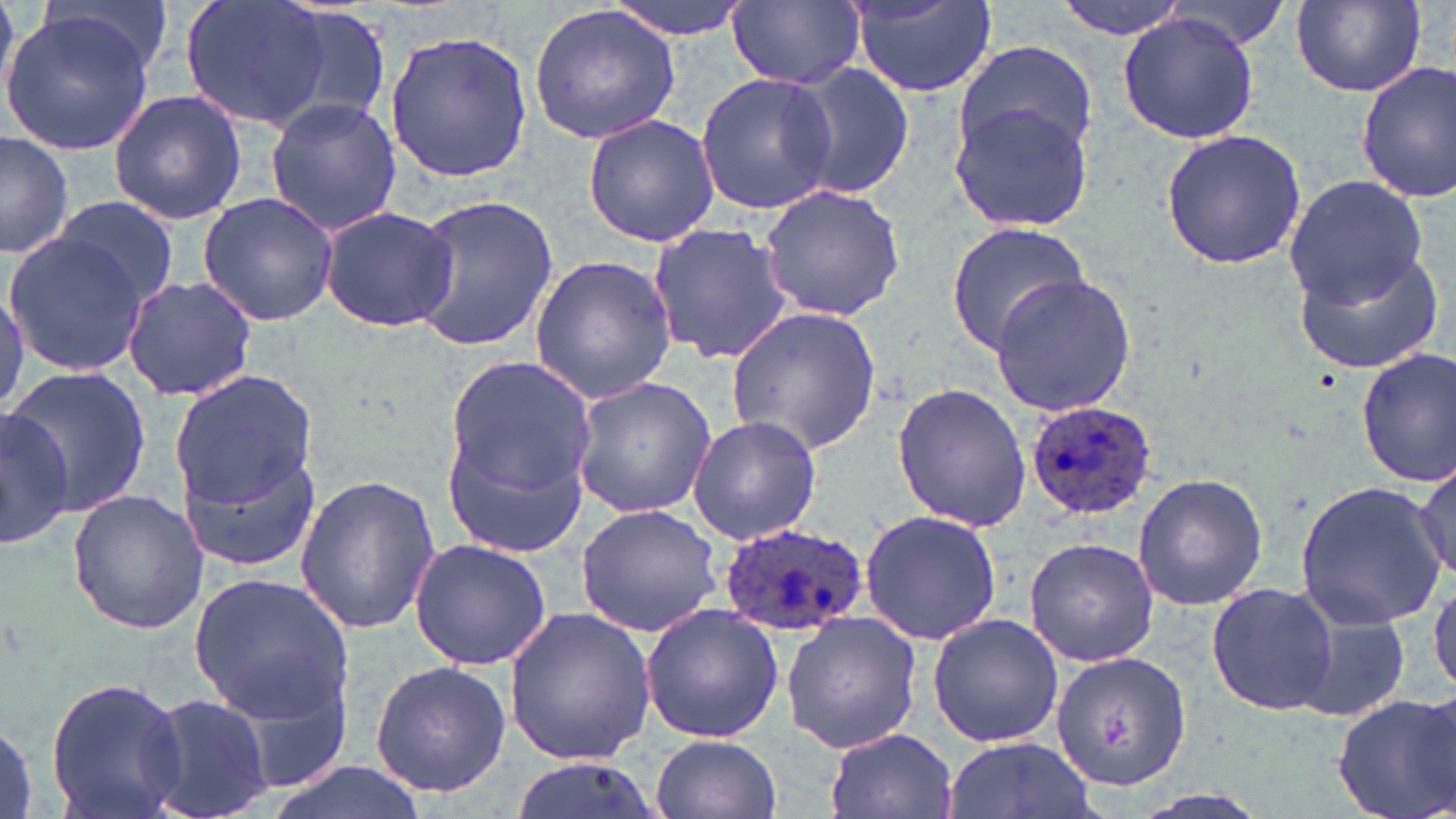
{
  "slide_level_diagnosis": "Plasmodium ovale",
  "field_of_view": "one of a larger specimen",
  "preparation": "thin blood film",
  "plasmodium_ovale_infected_red_blood_cell_locations": "approximate bounding boxes as [x1, y1, x2, y2] in pixels: [1024, 400, 1161, 520], [718, 520, 868, 637]",
  "modality": "light microscopy",
  "stain": "May-Grünwald-Giemsa",
  "uninfected_red_blood_cell_locations": "approximate bounding boxes as [x1, y1, x2, y2] in pixels: [0, 0, 27, 116], [182, 0, 335, 131], [601, 0, 754, 39], [1051, 0, 1193, 39], [1286, 0, 1429, 98], [727, 1, 864, 88], [851, 2, 995, 98], [1154, 3, 1297, 50], [528, 4, 683, 144], [275, 6, 395, 127], [2, 10, 157, 155], [1118, 11, 1258, 145], [385, 31, 533, 183], [953, 39, 1098, 162], [787, 61, 916, 201], [1356, 61, 1455, 205], [695, 71, 839, 214], [107, 90, 247, 225], [264, 98, 403, 235], [948, 98, 1096, 234], [581, 113, 721, 247], [1159, 128, 1308, 271], [0, 135, 75, 259], [1282, 174, 1430, 311], [757, 184, 907, 322], [196, 192, 340, 325], [406, 193, 558, 353], [51, 194, 180, 311], [319, 204, 460, 334], [647, 220, 793, 367], [942, 220, 1094, 356], [2, 226, 158, 378], [1292, 242, 1445, 373], [528, 255, 678, 405], [989, 273, 1136, 417], [121, 275, 258, 402], [727, 307, 882, 455], [1355, 349, 1455, 489], [438, 359, 595, 549], [8, 366, 151, 516], [169, 370, 320, 513], [571, 376, 717, 518], [889, 382, 1031, 532], [1, 403, 76, 550], [687, 415, 822, 543], [173, 417, 326, 581], [1414, 460, 1455, 583], [1132, 472, 1268, 612], [295, 474, 442, 635], [1294, 480, 1445, 630], [66, 489, 209, 635], [573, 503, 722, 638], [859, 508, 1002, 648], [410, 536, 552, 671], [1024, 537, 1159, 666], [189, 567, 356, 730], [1430, 579, 1456, 698], [1206, 581, 1340, 717], [640, 604, 784, 743], [502, 606, 658, 769], [1292, 606, 1416, 725], [781, 612, 921, 752], [927, 612, 1065, 749], [1048, 648, 1192, 793], [367, 658, 514, 800], [44, 675, 189, 819], [144, 691, 272, 819], [1332, 692, 1456, 819], [0, 715, 40, 819], [824, 728, 956, 819], [651, 734, 782, 819], [942, 735, 1099, 819], [252, 758, 435, 819]",
  "image_size": "1456×819 pixels",
  "magnification": "1000x"
}